Report the malaria status of this cell.
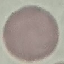
Uninfected.

Summary:
  - Stain: Giemsa
  - Capture: smartphone through the microscope eyepiece
  - Image type: automatically extracted cell patch, resized to 64 × 64 pixels
  - Preparation: thin smear